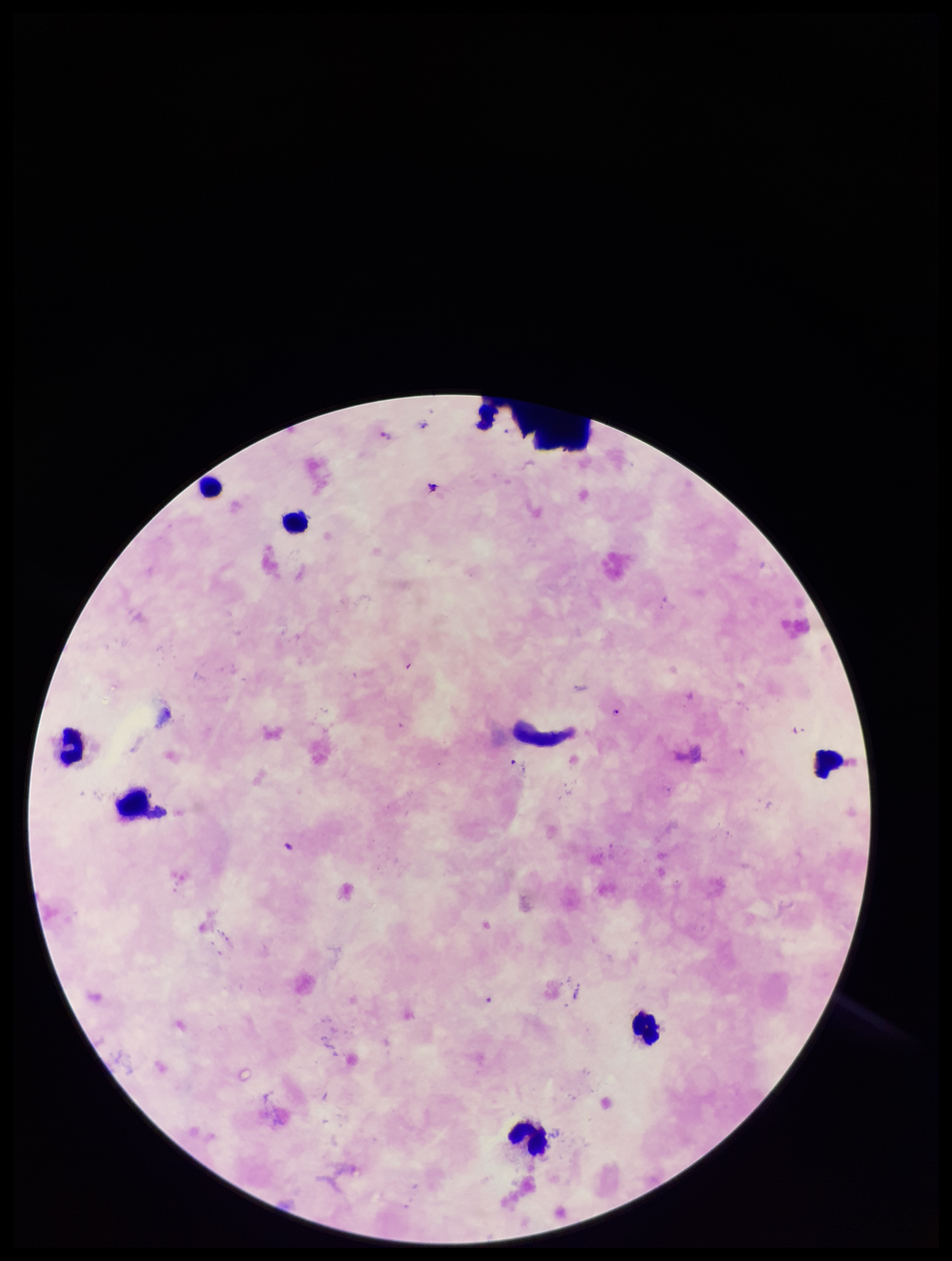
Patient malaria status: positive. Smartphone photograph taken through the eyepiece of a microscope. Species reported for this patient: Plasmodium falciparum. Parasite count: 4. Leukocyte count: 7. Single field of view. Preparation: thick blood smear. Image is 952×1261 pixels. Stained with Giemsa. Plasmodium parasites: identified.